Locate and identify every blood parasite.
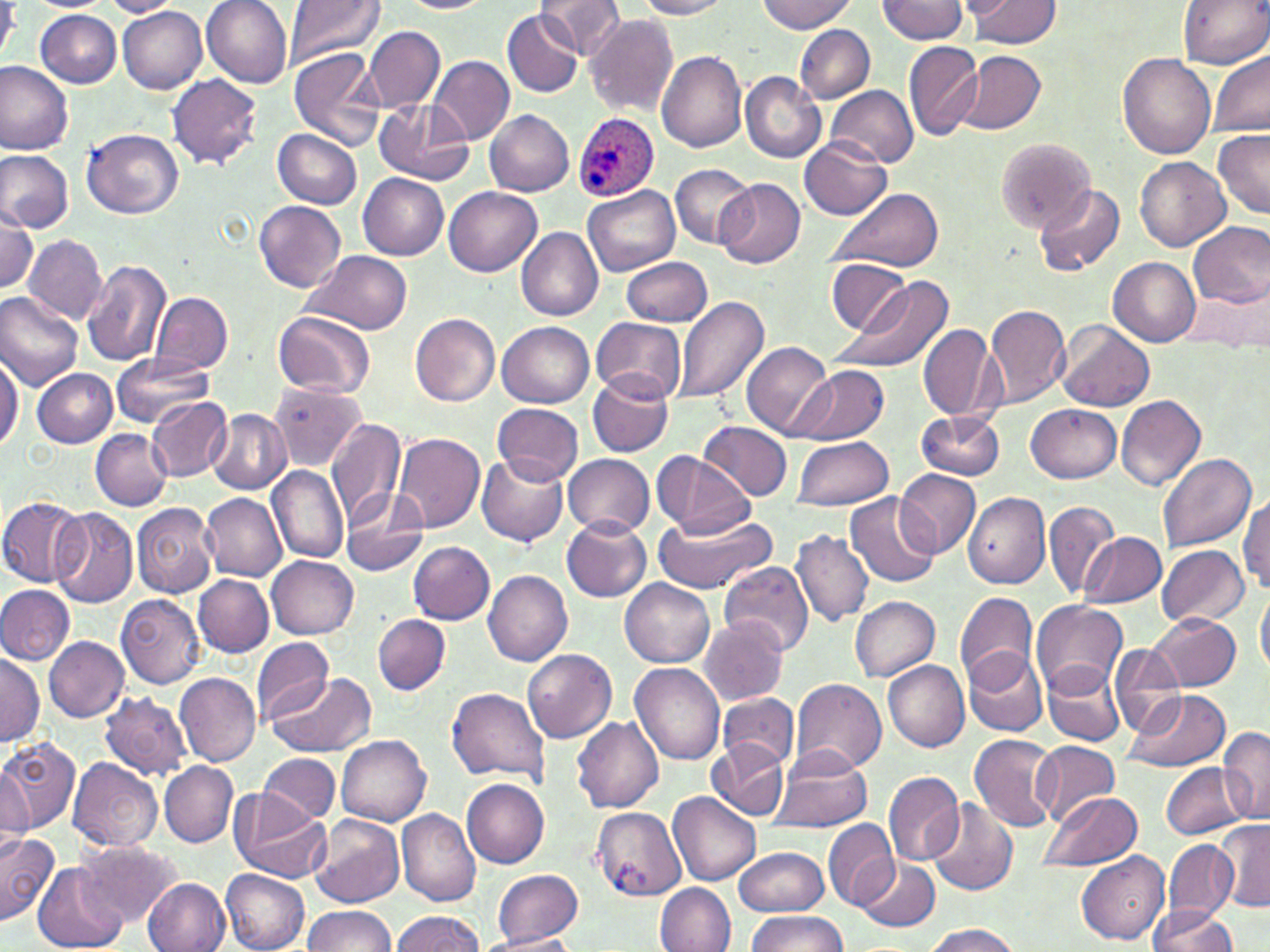

Approximate bounding boxes as named x1/y1/x2/y2 corners in pixels.
Plasmodium ovale-infected red blood cells: (x1=571, y1=111, x2=658, y2=201).
No Plasmodium falciparum, Plasmodium malariae, Plasmodium vivax, Babesia divergens, or Trypanosoma brucei observed.

Summary:
  - Uninfected red blood cell locations: (x1=201, y1=0, x2=293, y2=88), (x1=283, y1=0, x2=384, y2=69), (x1=537, y1=0, x2=625, y2=59), (x1=637, y1=0, x2=729, y2=19), (x1=758, y1=0, x2=856, y2=35), (x1=967, y1=0, x2=1062, y2=48), (x1=1178, y1=0, x2=1269, y2=68), (x1=100, y1=1, x2=182, y2=17), (x1=401, y1=1, x2=489, y2=14), (x1=878, y1=1, x2=971, y2=43), (x1=0, y1=2, x2=18, y2=64), (x1=118, y1=7, x2=208, y2=94), (x1=504, y1=9, x2=584, y2=98), (x1=36, y1=10, x2=121, y2=87), (x1=585, y1=14, x2=678, y2=117), (x1=794, y1=24, x2=874, y2=103), (x1=364, y1=26, x2=445, y2=112), (x1=904, y1=40, x2=983, y2=141), (x1=288, y1=46, x2=385, y2=151), (x1=1208, y1=48, x2=1270, y2=136), (x1=656, y1=51, x2=748, y2=152), (x1=958, y1=52, x2=1046, y2=136), (x1=1117, y1=53, x2=1215, y2=157), (x1=430, y1=55, x2=515, y2=145), (x1=0, y1=60, x2=73, y2=154), (x1=740, y1=72, x2=826, y2=162), (x1=167, y1=74, x2=262, y2=169), (x1=824, y1=85, x2=919, y2=169), (x1=374, y1=99, x2=475, y2=185), (x1=485, y1=110, x2=575, y2=197), (x1=82, y1=127, x2=185, y2=218), (x1=1211, y1=127, x2=1270, y2=217), (x1=273, y1=129, x2=362, y2=209), (x1=801, y1=138, x2=891, y2=219), (x1=994, y1=138, x2=1093, y2=230), (x1=0, y1=150, x2=73, y2=233), (x1=1134, y1=154, x2=1229, y2=252), (x1=669, y1=164, x2=754, y2=248), (x1=358, y1=173, x2=449, y2=260), (x1=715, y1=178, x2=807, y2=269), (x1=1033, y1=182, x2=1126, y2=277), (x1=581, y1=184, x2=680, y2=276), (x1=444, y1=187, x2=542, y2=276), (x1=831, y1=187, x2=942, y2=272), (x1=253, y1=200, x2=347, y2=291), (x1=0, y1=207, x2=37, y2=294), (x1=1187, y1=222, x2=1270, y2=308), (x1=516, y1=226, x2=603, y2=322), (x1=25, y1=235, x2=107, y2=324), (x1=302, y1=250, x2=413, y2=335), (x1=622, y1=256, x2=712, y2=326), (x1=1108, y1=256, x2=1200, y2=345), (x1=825, y1=258, x2=913, y2=336), (x1=81, y1=259, x2=171, y2=368), (x1=832, y1=275, x2=954, y2=374), (x1=1185, y1=283, x2=1268, y2=351), (x1=0, y1=289, x2=84, y2=389), (x1=152, y1=292, x2=232, y2=373), (x1=673, y1=294, x2=770, y2=405), (x1=985, y1=303, x2=1070, y2=407), (x1=272, y1=312, x2=376, y2=399), (x1=408, y1=312, x2=499, y2=406), (x1=593, y1=317, x2=686, y2=402), (x1=499, y1=321, x2=594, y2=406), (x1=1055, y1=321, x2=1154, y2=412), (x1=918, y1=325, x2=999, y2=421), (x1=741, y1=341, x2=834, y2=439), (x1=0, y1=349, x2=22, y2=454), (x1=109, y1=352, x2=212, y2=427), (x1=794, y1=365, x2=887, y2=445), (x1=32, y1=369, x2=117, y2=447), (x1=587, y1=372, x2=674, y2=456), (x1=268, y1=380, x2=366, y2=471), (x1=1116, y1=395, x2=1208, y2=493), (x1=145, y1=396, x2=231, y2=481), (x1=493, y1=402, x2=583, y2=486), (x1=1026, y1=404, x2=1120, y2=483), (x1=915, y1=409, x2=1007, y2=481), (x1=208, y1=410, x2=291, y2=494), (x1=327, y1=418, x2=405, y2=529), (x1=698, y1=420, x2=793, y2=501), (x1=90, y1=429, x2=172, y2=511), (x1=392, y1=432, x2=487, y2=534), (x1=791, y1=435, x2=896, y2=510), (x1=652, y1=451, x2=753, y2=539), (x1=475, y1=453, x2=569, y2=547), (x1=1158, y1=454, x2=1255, y2=551), (x1=564, y1=455, x2=655, y2=538), (x1=267, y1=466, x2=349, y2=564), (x1=894, y1=468, x2=980, y2=559), (x1=338, y1=489, x2=431, y2=577), (x1=201, y1=492, x2=287, y2=580), (x1=844, y1=492, x2=942, y2=588), (x1=962, y1=492, x2=1049, y2=590), (x1=1238, y1=495, x2=1270, y2=596), (x1=1, y1=497, x2=85, y2=585), (x1=1043, y1=498, x2=1121, y2=599), (x1=131, y1=503, x2=220, y2=598), (x1=48, y1=507, x2=138, y2=610), (x1=654, y1=510, x2=776, y2=596), (x1=562, y1=517, x2=652, y2=603), (x1=791, y1=530, x2=875, y2=627), (x1=1078, y1=531, x2=1166, y2=607), (x1=408, y1=541, x2=497, y2=624), (x1=1157, y1=545, x2=1249, y2=627), (x1=266, y1=556, x2=358, y2=638), (x1=718, y1=562, x2=816, y2=657), (x1=483, y1=569, x2=573, y2=666), (x1=192, y1=574, x2=274, y2=656), (x1=620, y1=578, x2=715, y2=669), (x1=1256, y1=584, x2=1269, y2=677), (x1=0, y1=585, x2=75, y2=665), (x1=956, y1=591, x2=1038, y2=689), (x1=117, y1=594, x2=205, y2=688), (x1=850, y1=596, x2=939, y2=680), (x1=1032, y1=600, x2=1128, y2=694), (x1=1149, y1=612, x2=1240, y2=691), (x1=373, y1=615, x2=450, y2=694), (x1=698, y1=616, x2=790, y2=706), (x1=43, y1=635, x2=129, y2=722), (x1=250, y1=636, x2=334, y2=724), (x1=1107, y1=642, x2=1187, y2=738), (x1=522, y1=648, x2=617, y2=743), (x1=964, y1=649, x2=1048, y2=736), (x1=0, y1=653, x2=43, y2=747), (x1=883, y1=660, x2=969, y2=750), (x1=1042, y1=661, x2=1127, y2=746), (x1=630, y1=663, x2=724, y2=765), (x1=267, y1=672, x2=376, y2=758), (x1=174, y1=673, x2=261, y2=768), (x1=788, y1=679, x2=887, y2=778), (x1=446, y1=687, x2=552, y2=783), (x1=1122, y1=689, x2=1230, y2=773), (x1=100, y1=691, x2=192, y2=781), (x1=718, y1=692, x2=799, y2=770), (x1=572, y1=716, x2=664, y2=813), (x1=1217, y1=727, x2=1270, y2=823), (x1=969, y1=734, x2=1062, y2=833), (x1=337, y1=736, x2=431, y2=826), (x1=1, y1=738, x2=81, y2=832), (x1=708, y1=740, x2=787, y2=819), (x1=1031, y1=741, x2=1119, y2=824), (x1=771, y1=749, x2=871, y2=833), (x1=258, y1=754, x2=339, y2=825), (x1=68, y1=757, x2=163, y2=852), (x1=159, y1=762, x2=237, y2=847), (x1=1162, y1=762, x2=1252, y2=839), (x1=0, y1=766, x2=35, y2=853), (x1=883, y1=771, x2=965, y2=866), (x1=461, y1=778, x2=550, y2=866), (x1=1037, y1=791, x2=1141, y2=871), (x1=668, y1=792, x2=760, y2=886), (x1=231, y1=793, x2=330, y2=884), (x1=926, y1=799, x2=1018, y2=896), (x1=590, y1=806, x2=686, y2=899), (x1=397, y1=807, x2=481, y2=907), (x1=310, y1=815, x2=404, y2=910), (x1=822, y1=818, x2=900, y2=910), (x1=1216, y1=819, x2=1269, y2=912), (x1=0, y1=830, x2=58, y2=924), (x1=1162, y1=838, x2=1236, y2=925), (x1=76, y1=839, x2=181, y2=926), (x1=734, y1=845, x2=830, y2=917), (x1=1075, y1=850, x2=1170, y2=944), (x1=853, y1=857, x2=940, y2=934), (x1=32, y1=864, x2=128, y2=952), (x1=493, y1=869, x2=583, y2=945), (x1=220, y1=870, x2=310, y2=952), (x1=142, y1=878, x2=230, y2=952), (x1=656, y1=882, x2=735, y2=952), (x1=302, y1=906, x2=397, y2=952), (x1=1148, y1=906, x2=1239, y2=952), (x1=391, y1=911, x2=483, y2=951), (x1=745, y1=911, x2=848, y2=952), (x1=921, y1=923, x2=1022, y2=952), (x1=475, y1=933, x2=583, y2=952)
  - Slide-level diagnosis: Plasmodium ovale
  - Magnification: 1000x
  - Image size: 1270×952 pixels
  - Modality: light microscopy
  - Field of view: single
  - Stain: May-Grünwald-Giemsa
  - Preparation: thin blood film